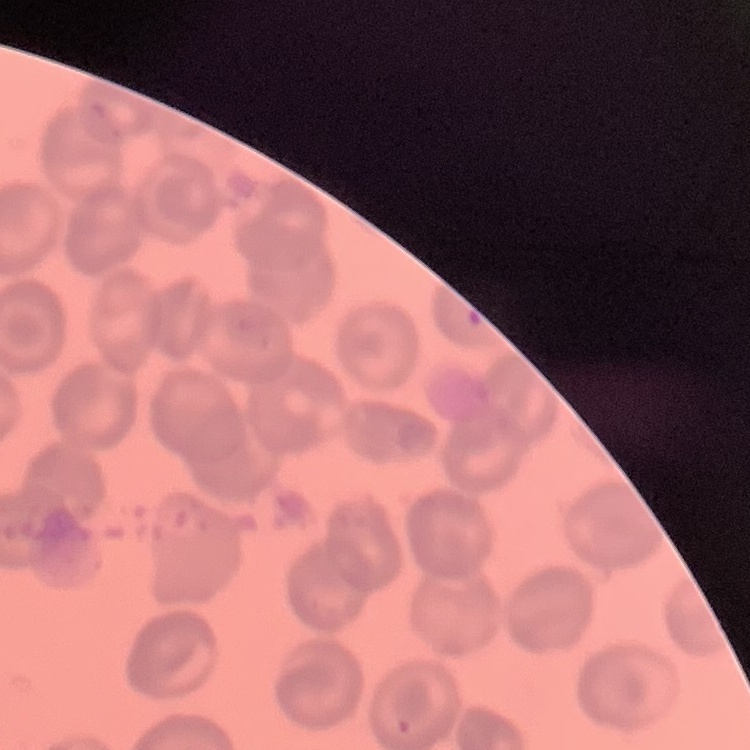

Summary:
  - Erythrocyte morphology: no rouleaux formation
  - Stain: Field's or Giemsa
  - Preparation: thin blood film
  - Image type: square crop of a larger photomicrograph